Identify the parasite.
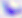
This is Toxoplasma gondii.

magnification = 400x
modality = photomicrograph